Locate every blood parasite and identify its species.
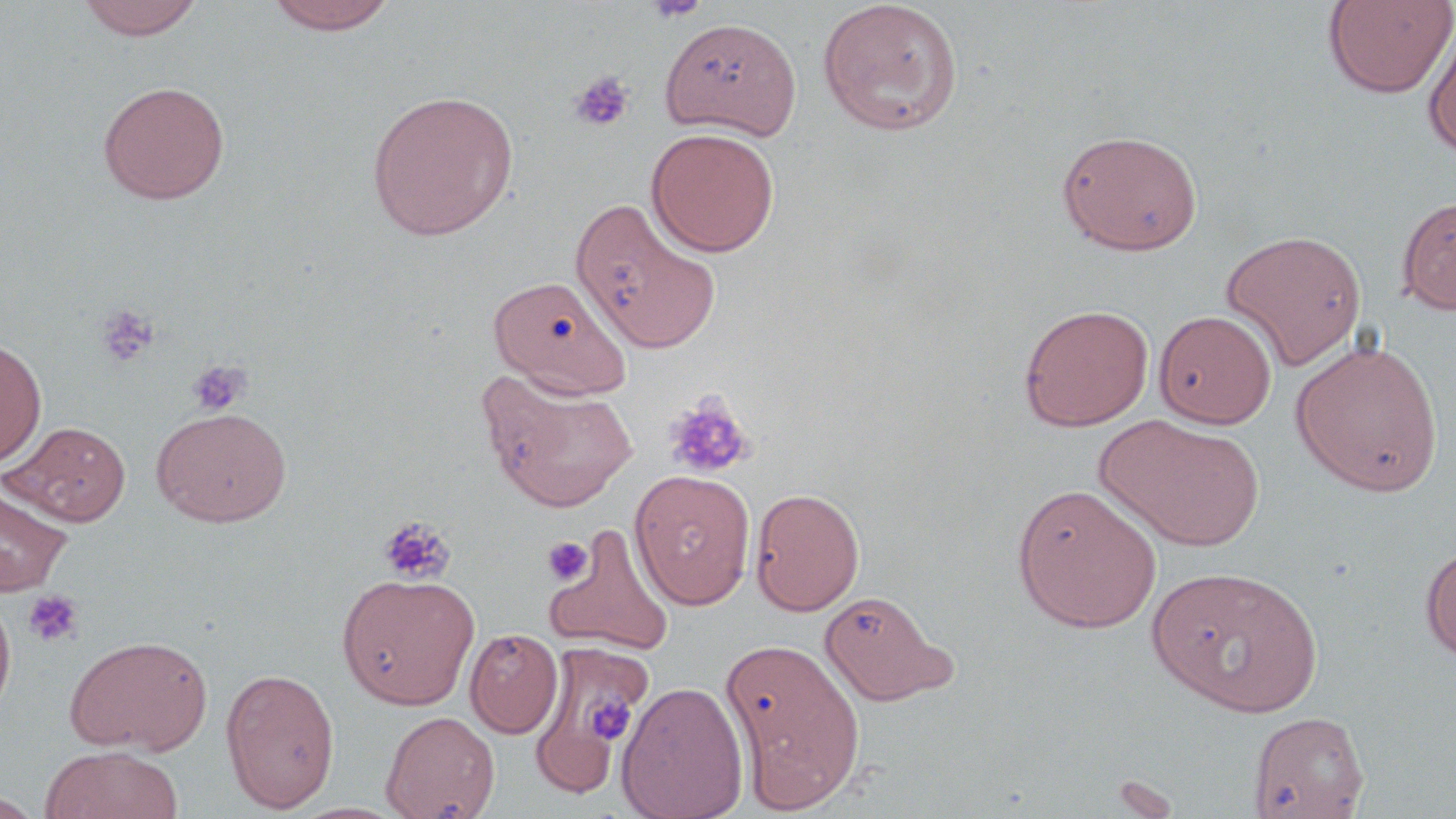

No blood parasites observed.

slide-level diagnosis = negative for blood parasites
uninfected red blood cell locations = approximate bounding boxes as named x1/y1/x2/y2 corners in pixels: (x1=76, y1=0, x2=205, y2=40), (x1=264, y1=0, x2=399, y2=35), (x1=1322, y1=0, x2=1455, y2=99), (x1=817, y1=1, x2=964, y2=137), (x1=1422, y1=19, x2=1456, y2=159), (x1=659, y1=23, x2=802, y2=147), (x1=97, y1=80, x2=230, y2=204), (x1=365, y1=90, x2=519, y2=240), (x1=646, y1=127, x2=780, y2=256), (x1=1057, y1=129, x2=1203, y2=255), (x1=1396, y1=194, x2=1456, y2=315), (x1=570, y1=197, x2=720, y2=354), (x1=1220, y1=228, x2=1367, y2=371), (x1=488, y1=274, x2=632, y2=398), (x1=1019, y1=303, x2=1154, y2=431), (x1=1154, y1=309, x2=1276, y2=429), (x1=0, y1=337, x2=47, y2=468), (x1=1291, y1=338, x2=1444, y2=497), (x1=479, y1=370, x2=637, y2=513), (x1=151, y1=406, x2=291, y2=527), (x1=1096, y1=414, x2=1266, y2=551), (x1=3, y1=421, x2=131, y2=526), (x1=629, y1=469, x2=756, y2=610), (x1=0, y1=482, x2=72, y2=597), (x1=1012, y1=482, x2=1163, y2=633), (x1=750, y1=487, x2=865, y2=616), (x1=544, y1=526, x2=676, y2=656), (x1=1420, y1=545, x2=1456, y2=663), (x1=1145, y1=564, x2=1324, y2=717), (x1=336, y1=572, x2=480, y2=709), (x1=819, y1=588, x2=957, y2=707), (x1=0, y1=595, x2=16, y2=723), (x1=465, y1=628, x2=563, y2=738), (x1=64, y1=634, x2=214, y2=756), (x1=721, y1=637, x2=867, y2=811), (x1=220, y1=666, x2=340, y2=813), (x1=616, y1=681, x2=748, y2=819), (x1=381, y1=710, x2=499, y2=818), (x1=1246, y1=710, x2=1370, y2=818), (x1=533, y1=715, x2=618, y2=798), (x1=39, y1=745, x2=184, y2=819), (x1=0, y1=791, x2=45, y2=817)
field of view = one of a larger specimen
image size = 1456×819 pixels
modality = light microscopy
preparation = thin blood film
stain = May-Grünwald-Giemsa
platelet locations = approximate bounding boxes as named x1/y1/x2/y2 corners in pixels: (x1=646, y1=0, x2=709, y2=23), (x1=569, y1=70, x2=634, y2=132), (x1=96, y1=304, x2=160, y2=368), (x1=186, y1=360, x2=251, y2=417), (x1=663, y1=392, x2=754, y2=480), (x1=377, y1=514, x2=455, y2=585), (x1=542, y1=536, x2=593, y2=585), (x1=23, y1=590, x2=84, y2=648), (x1=585, y1=695, x2=635, y2=742)
magnification = 1000x